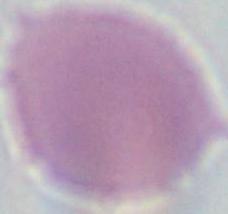

identification = erythrocyte
magnification = 1000x
modality = photomicrograph